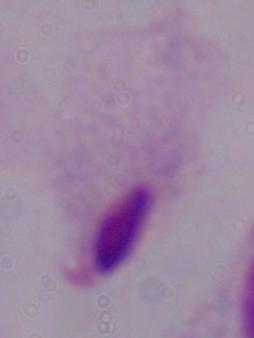
magnification = 1000x
modality = photomicrograph
identification = trichomonad